Report the malaria status of this cell.
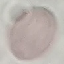

Uninfected.

Summary:
  - Capture: smartphone through the microscope eyepiece
  - Image type: cell patch, automatically extracted from a larger field of view and resized to 64 × 64 pixels
  - Stain: Giemsa
  - Preparation: thin smear